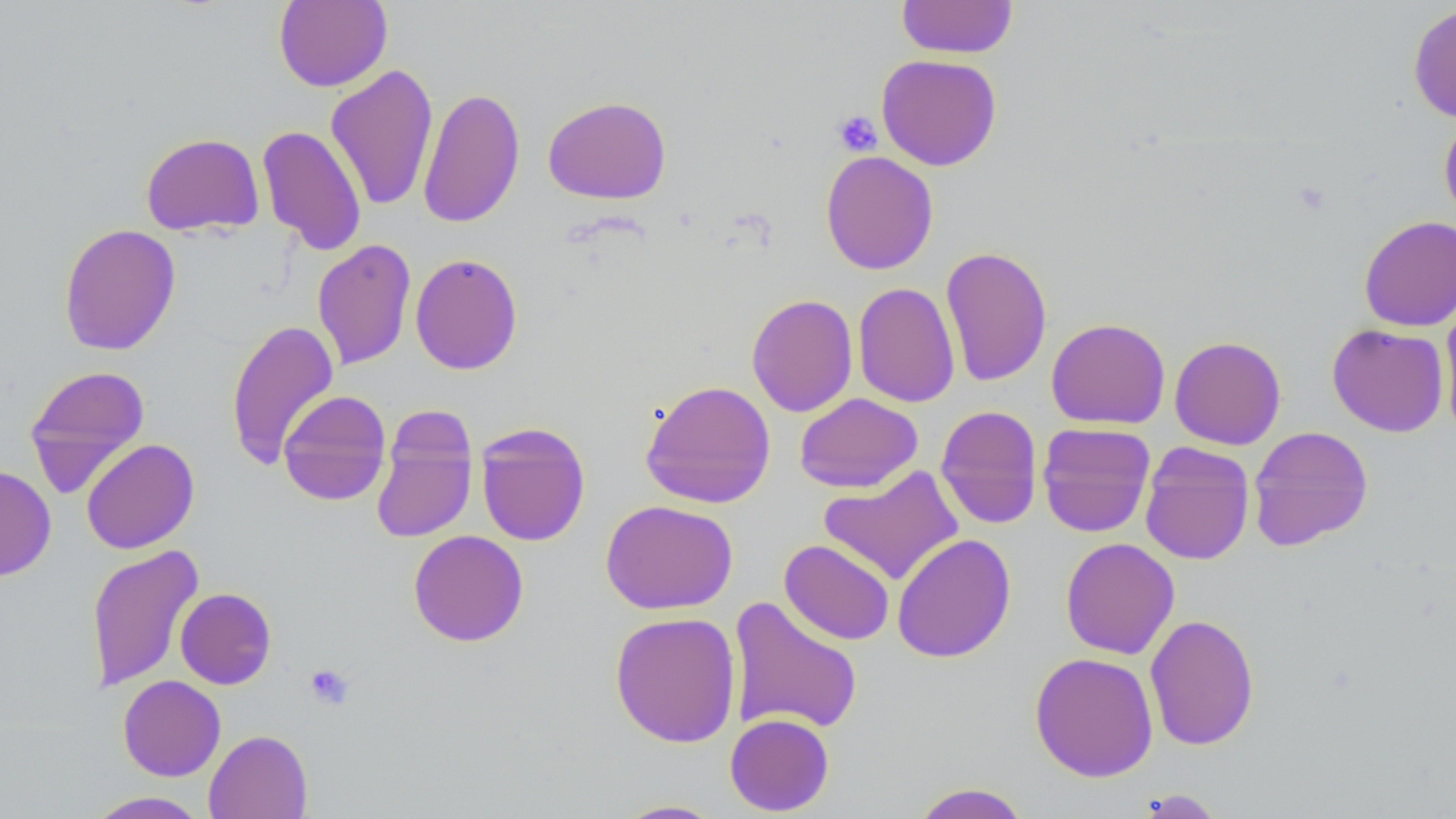

slide-level diagnosis = no evidence of blood parasites
field of view = single
modality = light microscopy
image size = 1456×819 pixels
stain = May-Grünwald-Giemsa
platelet locations = approximate bounding boxes as [x1, y1, x2, y2] in pixels: [832, 111, 882, 156], [304, 664, 353, 709]
magnification = 1000x
uninfected red blood cell locations = approximate bounding boxes as [x1, y1, x2, y2] in pixels: [273, 0, 392, 91], [897, 0, 1018, 59], [1407, 3, 1456, 123], [876, 54, 1002, 171], [325, 64, 439, 212], [418, 86, 526, 229], [543, 95, 672, 204], [1439, 114, 1456, 224], [257, 124, 367, 255], [141, 132, 264, 236], [820, 150, 939, 274], [1358, 215, 1456, 332], [58, 223, 181, 356], [312, 239, 416, 370], [940, 245, 1053, 387], [409, 253, 523, 375], [852, 282, 960, 408], [746, 294, 858, 417], [1439, 296, 1456, 439], [1046, 317, 1171, 429], [225, 318, 340, 469], [1327, 323, 1449, 436], [1169, 335, 1286, 449], [23, 365, 151, 495], [640, 379, 776, 509], [278, 390, 392, 505], [795, 393, 923, 493], [935, 405, 1043, 529], [371, 410, 478, 545], [475, 422, 590, 546], [1037, 422, 1155, 537], [1248, 425, 1373, 551], [81, 438, 200, 554], [1139, 442, 1255, 565], [0, 464, 57, 581], [819, 466, 964, 586], [600, 500, 738, 614], [408, 529, 529, 647], [891, 533, 1017, 663], [1060, 537, 1179, 659], [779, 539, 895, 646], [86, 544, 204, 692], [175, 588, 277, 689], [727, 596, 864, 736], [609, 611, 741, 748], [1145, 613, 1260, 751], [1030, 651, 1158, 782], [118, 675, 226, 781], [724, 713, 834, 816], [204, 729, 313, 819], [910, 782, 1031, 819], [1133, 789, 1228, 818], [86, 791, 209, 818], [612, 798, 727, 818]
preparation = thin blood smear